Name the blood parasite species.
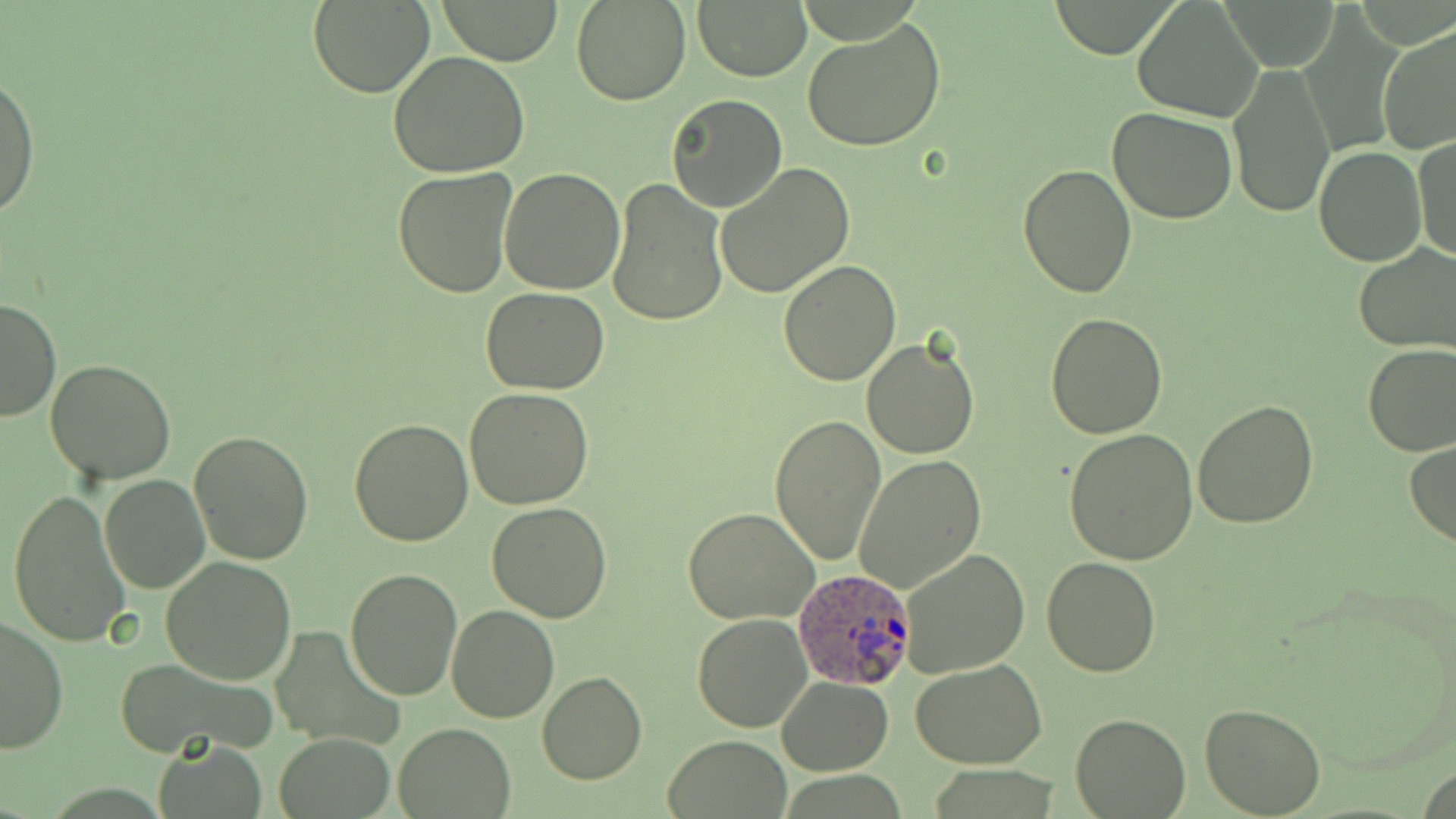

Plasmodium ovale.

field of view = one of a larger specimen
magnification = 1000x
uninfected red blood cell locations = approximate bounding boxes as [x1, y1, x2, y2] in pixels: [434, 0, 563, 66], [571, 0, 691, 105], [307, 1, 438, 99], [1132, 1, 1262, 121], [694, 3, 810, 80], [803, 18, 946, 153], [1377, 24, 1456, 157], [388, 51, 531, 177], [1228, 63, 1336, 218], [0, 73, 38, 221], [666, 94, 787, 212], [1107, 108, 1239, 224], [1414, 138, 1455, 263], [1313, 145, 1425, 265], [714, 163, 855, 298], [1017, 163, 1139, 297], [392, 166, 519, 299], [499, 167, 626, 296], [606, 178, 728, 327], [1354, 245, 1455, 354], [778, 259, 902, 385], [481, 287, 610, 394], [0, 298, 62, 424], [1045, 313, 1169, 439], [862, 337, 979, 458], [1362, 343, 1456, 455], [45, 358, 177, 485], [464, 387, 594, 509], [1192, 400, 1319, 529], [768, 413, 887, 563], [348, 418, 474, 546], [187, 429, 313, 566], [1064, 429, 1198, 565], [1406, 439, 1456, 547], [855, 455, 986, 592], [99, 473, 209, 592], [8, 488, 133, 648], [486, 502, 614, 622], [684, 508, 819, 625], [898, 547, 1030, 677], [161, 556, 297, 684], [1042, 557, 1160, 677], [345, 566, 463, 700], [446, 604, 559, 723], [692, 614, 813, 731], [1, 615, 69, 753], [271, 625, 403, 749], [113, 659, 273, 757], [910, 660, 1046, 769], [537, 670, 647, 785], [776, 676, 892, 774], [1200, 703, 1326, 818], [1069, 713, 1191, 816], [394, 722, 514, 817], [273, 733, 397, 818], [663, 734, 792, 819], [158, 741, 267, 818]
image size = 1456×819 pixels
modality = light microscopy
stain = May-Grünwald-Giemsa
Plasmodium ovale-infected red blood cell locations = approximate bounding boxes as [x1, y1, x2, y2] in pixels: [793, 566, 914, 688]
preparation = thin blood film